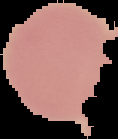

image size = 118×139 pixels
preparation = thin blood smear
image type = cell region segmented out of the field of view; surrounding area masked to black
result = no malaria parasites seen